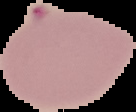

Segmented cell region on a black background. Result: malaria parasites identified. From a thin blood smear. Image is 136×112 pixels.